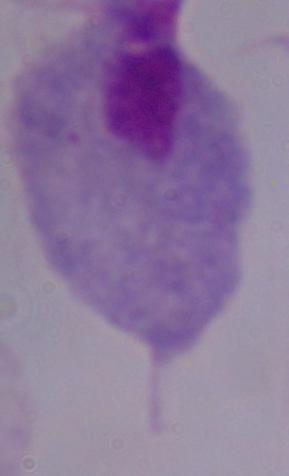

magnification = 1000x
modality = micrograph
identification = trichomonad